Assess this cell for malaria.
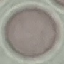
Uninfected.

{
  "image_type": "cell patch, automatically extracted from a larger field of view and resized to 64 × 64 pixels",
  "preparation": "thin blood smear",
  "stain": "Giemsa",
  "capture": "smartphone through the microscope eyepiece"
}